Locate every Plasmodium falciparum-infected red blood cell.
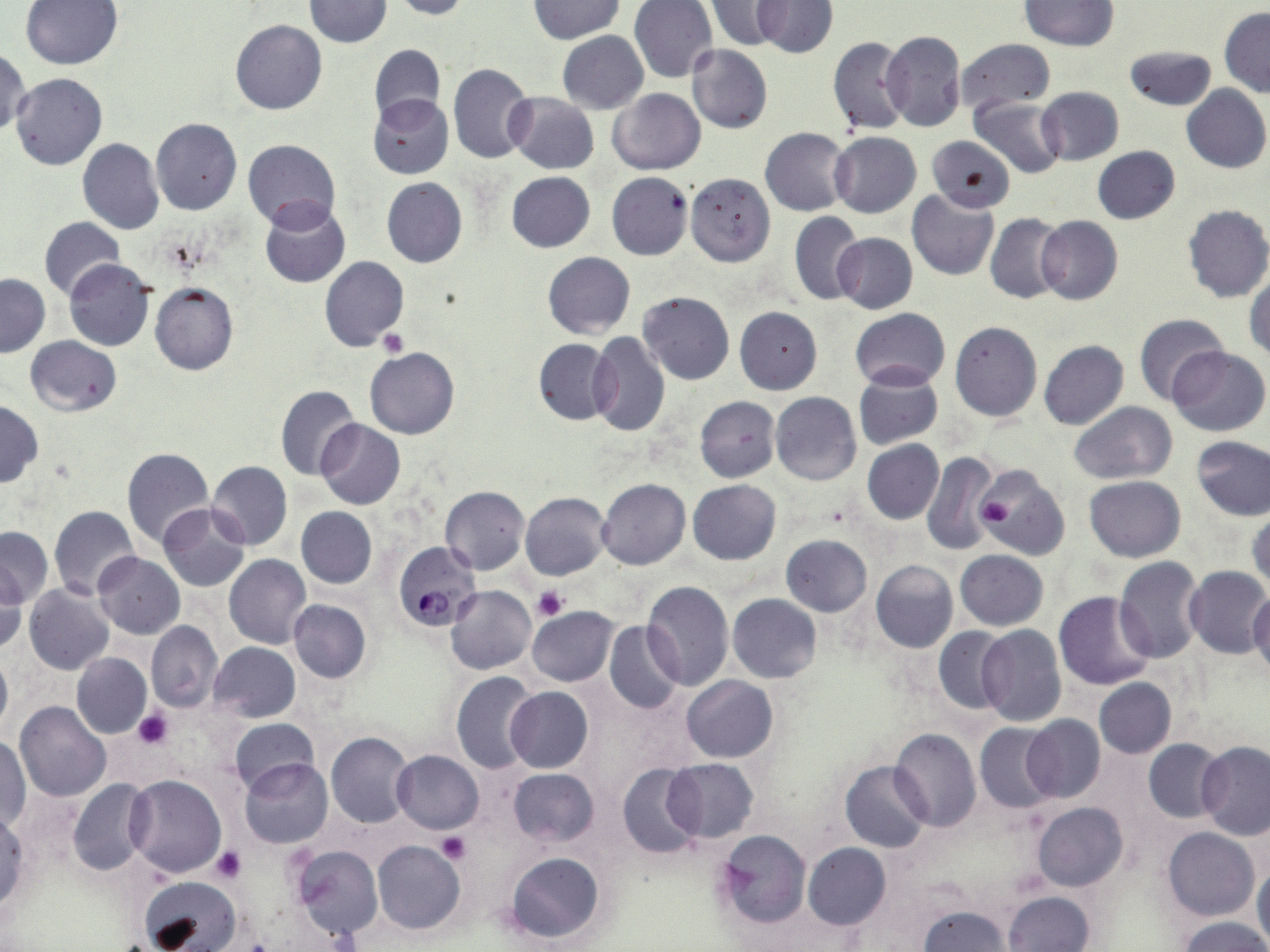

Approximate bounding boxes as [x1, y1, x2, y2] in pixels.
Plasmodium falciparum-infected red blood cells: [391, 541, 482, 632].

slide-level diagnosis = Plasmodium falciparum
image size = 1270×952 pixels
modality = light microscopy
uninfected red blood cell locations = approximate bounding boxes as [x1, y1, x2, y2] in pixels: [21, 0, 123, 71], [304, 0, 391, 47], [392, 0, 473, 20], [629, 0, 719, 84], [753, 0, 836, 58], [1018, 0, 1118, 49], [529, 1, 624, 43], [705, 2, 791, 52], [1220, 7, 1270, 97], [231, 20, 327, 115], [881, 30, 966, 132], [558, 32, 648, 113], [828, 37, 911, 136], [955, 39, 1055, 115], [368, 43, 445, 124], [687, 44, 772, 134], [1125, 44, 1216, 111], [1, 46, 31, 137], [447, 63, 535, 164], [11, 73, 107, 171], [1182, 84, 1270, 174], [1037, 87, 1124, 166], [609, 88, 704, 175], [506, 93, 599, 174], [367, 94, 453, 179], [970, 97, 1066, 179], [151, 117, 242, 215], [760, 128, 852, 216], [830, 131, 921, 218], [927, 136, 1015, 213], [78, 138, 164, 235], [244, 139, 340, 230], [1092, 146, 1180, 224], [507, 172, 595, 252], [606, 172, 694, 260], [684, 172, 776, 266], [382, 177, 467, 267], [907, 189, 999, 280], [259, 200, 349, 287], [1182, 204, 1270, 304], [790, 211, 864, 305], [986, 213, 1068, 304], [40, 215, 125, 303], [1036, 216, 1123, 305], [833, 233, 917, 314], [543, 252, 635, 339], [320, 256, 409, 352], [64, 258, 156, 351], [1246, 270, 1270, 360], [0, 273, 49, 357], [149, 282, 238, 376], [637, 292, 735, 384], [734, 306, 822, 394], [849, 308, 950, 391], [1133, 313, 1228, 406], [950, 322, 1042, 421], [589, 333, 671, 437], [26, 336, 120, 415], [533, 338, 617, 426], [1039, 340, 1128, 431], [366, 347, 458, 439], [1168, 347, 1268, 437], [853, 369, 943, 449], [276, 384, 361, 480], [769, 392, 862, 486], [694, 396, 780, 482], [0, 400, 43, 488], [1068, 402, 1177, 483], [316, 419, 405, 510], [1191, 437, 1270, 521], [861, 440, 943, 524], [121, 446, 213, 547], [921, 451, 999, 555], [208, 461, 292, 550], [977, 464, 1071, 560], [1085, 476, 1186, 561], [597, 478, 690, 569], [688, 479, 781, 564], [441, 485, 529, 573], [520, 492, 610, 580], [157, 502, 250, 591], [49, 505, 140, 600], [1247, 506, 1270, 598], [296, 507, 377, 588], [0, 527, 52, 608], [782, 535, 872, 615], [954, 549, 1048, 630], [93, 553, 184, 639], [224, 554, 311, 648], [1114, 557, 1207, 662], [870, 560, 958, 653], [0, 565, 27, 653], [1183, 566, 1270, 659], [642, 581, 734, 690], [23, 585, 116, 675], [446, 585, 537, 675], [1054, 590, 1158, 691], [1249, 591, 1270, 679], [727, 594, 822, 683], [288, 599, 371, 683], [528, 606, 619, 686], [530, 617, 680, 700], [604, 619, 684, 714], [147, 621, 222, 712], [976, 625, 1067, 726], [932, 627, 1011, 716], [71, 641, 221, 726], [209, 642, 300, 722], [0, 649, 11, 736], [72, 652, 151, 738], [452, 672, 540, 773], [682, 675, 777, 762], [1093, 678, 1176, 758], [504, 686, 593, 772], [15, 701, 110, 801], [1022, 714, 1106, 803], [228, 719, 319, 796], [974, 722, 1062, 814], [890, 728, 982, 831], [326, 732, 414, 829], [1, 736, 31, 830], [1144, 739, 1227, 823], [1196, 741, 1270, 839], [391, 750, 483, 833], [240, 758, 333, 849], [663, 758, 758, 843], [841, 761, 931, 852], [618, 762, 705, 859], [508, 768, 599, 847], [124, 774, 226, 878], [68, 779, 154, 876], [1032, 802, 1128, 891], [0, 811, 28, 913], [1162, 828, 1258, 921], [715, 829, 811, 928], [373, 840, 465, 934], [803, 842, 890, 929], [292, 845, 382, 940], [505, 852, 604, 944], [1254, 861, 1270, 946], [140, 876, 241, 952], [1002, 891, 1094, 952], [917, 905, 1010, 951], [1174, 916, 1270, 952]
magnification = 1000x
platelet locations = approximate bounding boxes as [x1, y1, x2, y2] in pixels: [378, 329, 406, 356], [974, 479, 1042, 550], [980, 496, 1012, 529], [534, 586, 568, 621], [133, 709, 172, 748], [436, 833, 472, 864], [211, 847, 246, 883]
preparation = thin blood film
field of view = single
stain = May-Grünwald-Giemsa